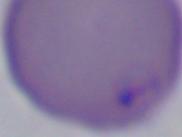
Micrograph. Captured at 1000x magnification. A Babesia parasite is shown.